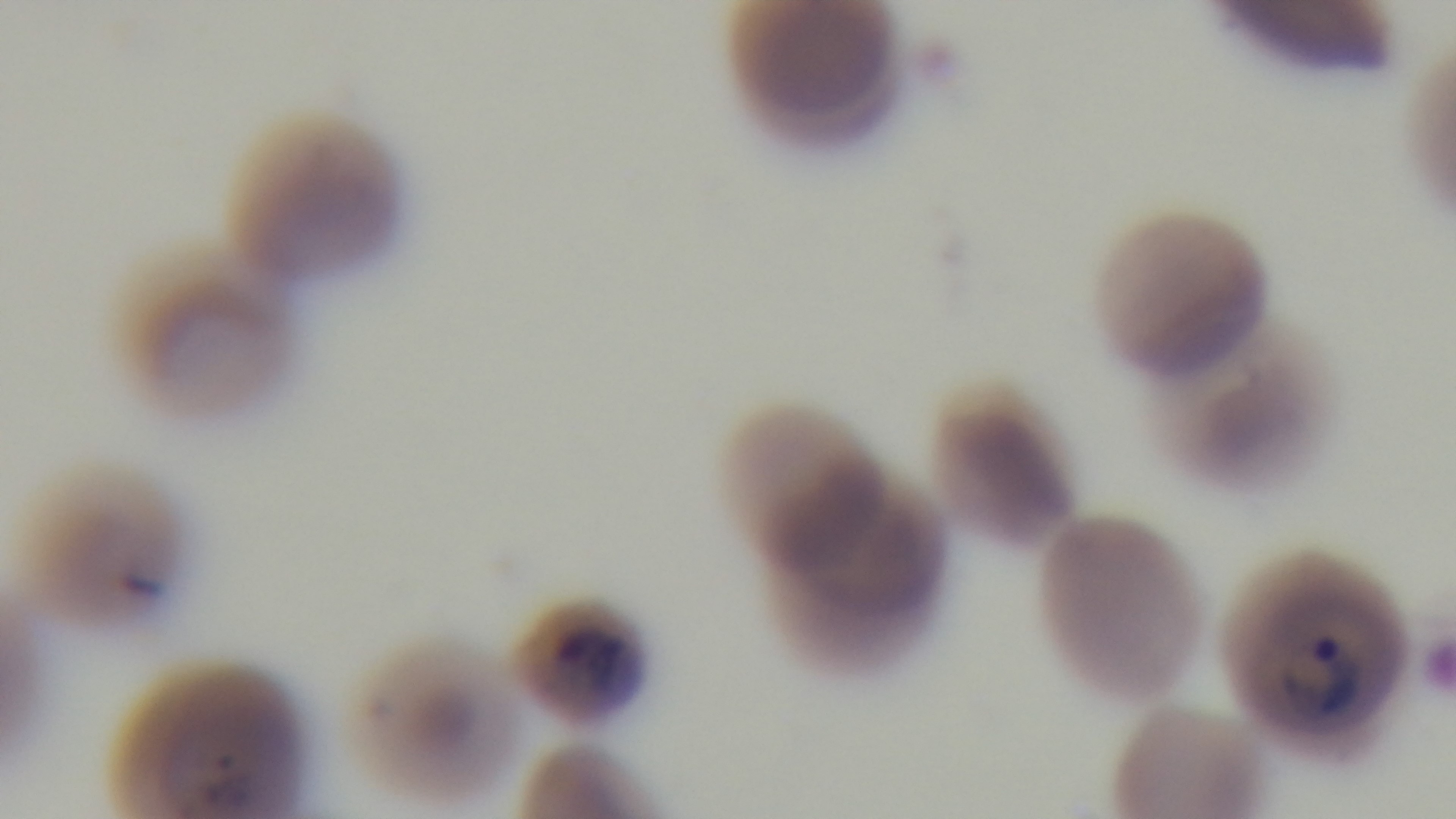
Oil-immersion objective, 100x. Malaria status: positive. Preparation: thin blood film. One field from the slide. Light microscopy. Captured with a mounted 4K digital camera. Giemsa-stained.